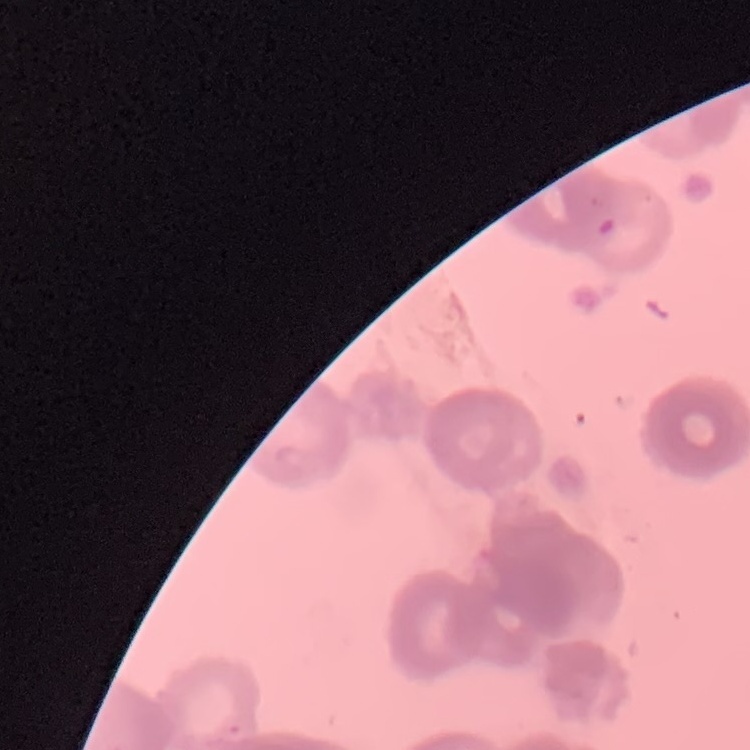
Summary:
  - Red blood cell morphology: rouleaux formation
  - Image type: one tile cut from a larger photomicrograph
  - Stain: Field's or Giemsa
  - Preparation: thin peripheral smear